Name the parasite shown.
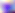
This is Toxoplasma gondii.

magnification: 400x
modality: photomicrograph